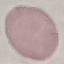
malaria status = uninfected
capture = smartphone through the microscope eyepiece
image type = cell patch, automatically extracted from a larger field of view and resized to 64 × 64 pixels
stain = Giemsa
preparation = thin blood smear